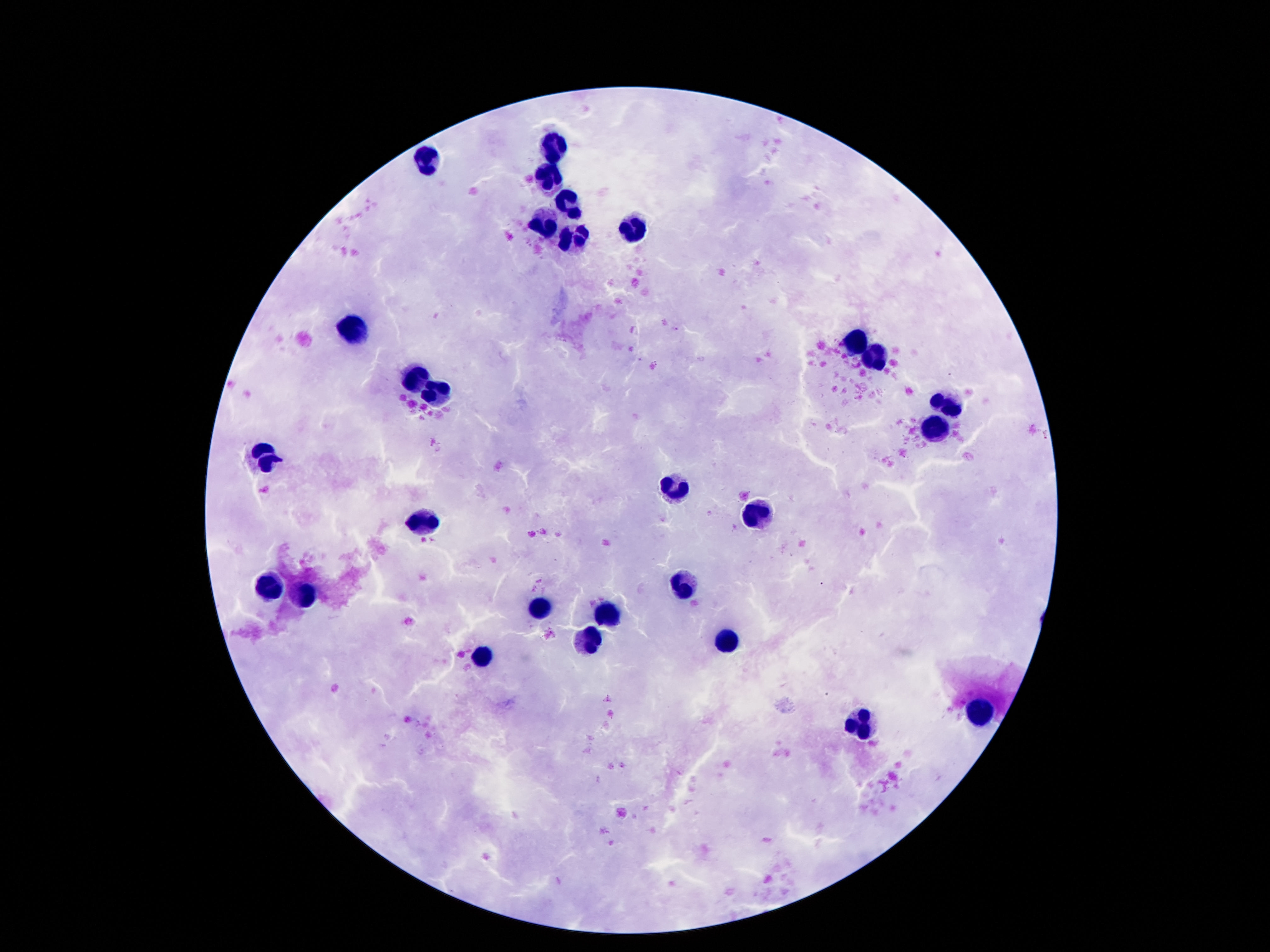

Approximate centers as {x, y} in pixels. Leukocyte locations: {557, 146}, {427, 156}, {546, 175}, {570, 206}, {545, 222}, {635, 232}, {572, 238}, {353, 328}, {859, 340}, {874, 362}, {413, 378}, {435, 393}, {947, 400}, {935, 427}, {264, 453}, {675, 484}, {757, 515}, {427, 522}, {269, 584}, {684, 586}, {304, 598}, {542, 609}, {608, 614}, {588, 640}, {729, 640}, {481, 658}, {981, 711}, {863, 724}. Image is 1270×952 pixels. Patient malaria status: negative. Single field of view. 100x magnification. Giemsa stain. Thick blood smear. Photographed through the microscope eyepiece with a smartphone camera.